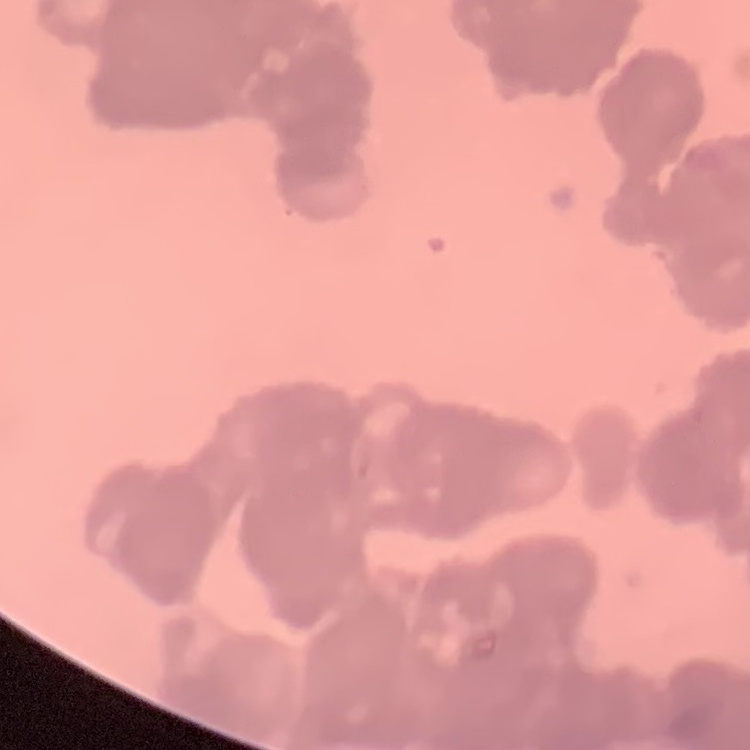

erythrocyte morphology = rouleaux formation
preparation = thin blood film
image type = square crop of a larger photomicrograph
stain = Field's or Giemsa